Classify this cell by malaria status.
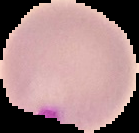

It is parasitized.

{
  "image_type": "segmented cell region on a black background",
  "preparation": "thin blood smear",
  "image_size": "139×133 pixels"
}